Point out every Plasmodium parasite.
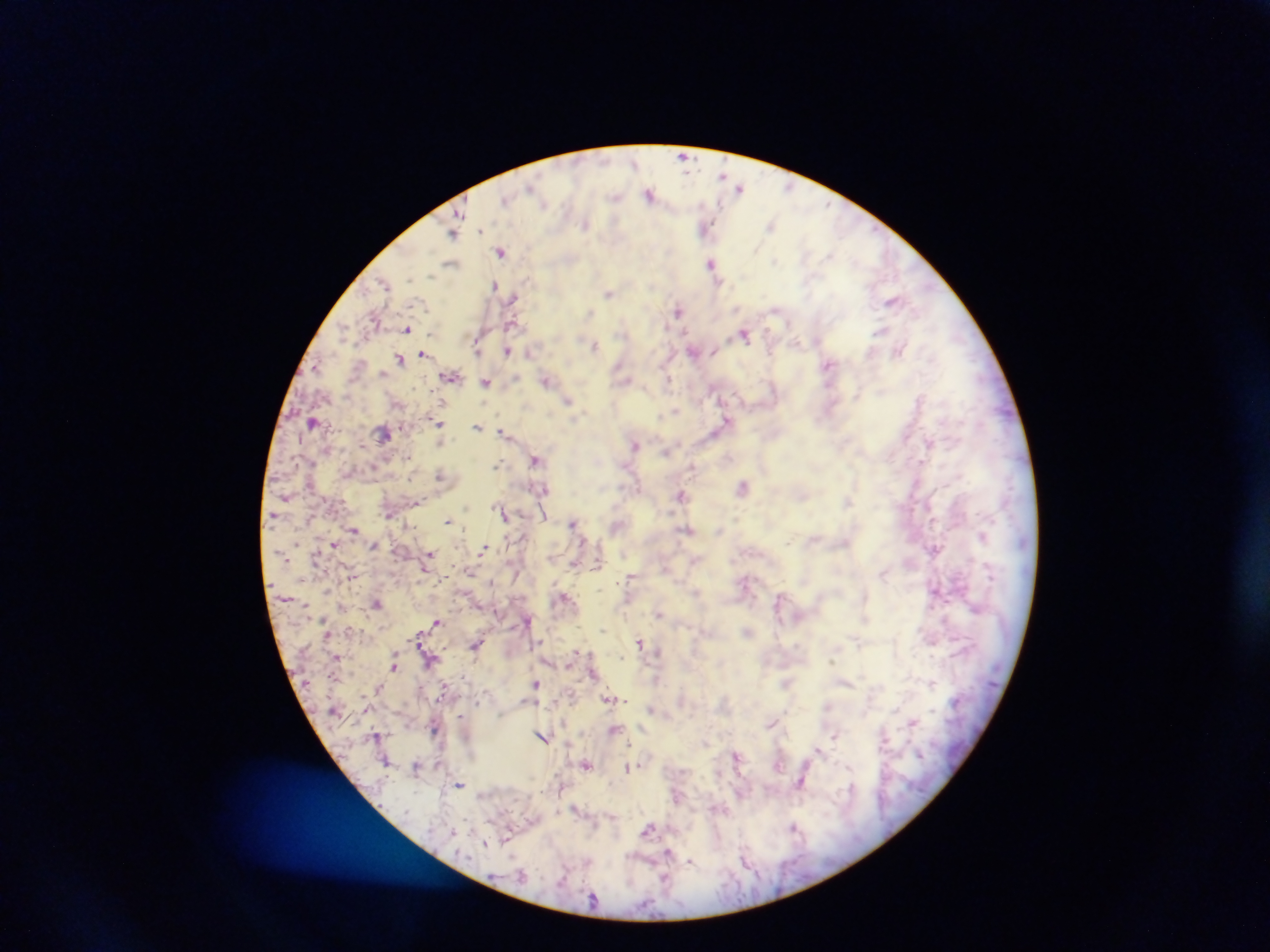

Approximate centers as (x, y) in pixels.
Plasmodium parasites: (684, 155), (634, 163), (722, 175), (789, 187), (740, 188), (650, 194), (615, 196), (827, 204), (585, 223), (771, 225), (706, 228), (453, 234), (502, 251), (775, 260), (712, 263), (451, 264), (430, 276), (384, 283), (494, 285), (609, 294), (512, 298), (892, 301), (737, 309), (775, 309), (679, 310), (589, 314), (511, 324), (406, 329), (881, 330), (743, 336), (595, 346), (507, 351), (899, 351), (530, 352), (694, 352), (423, 353), (400, 359), (829, 366), (316, 367), (451, 377), (667, 379), (546, 381), (485, 383), (857, 395), (568, 400), (675, 410), (727, 421), (438, 422), (477, 427), (503, 430), (929, 443), (635, 444), (666, 452), (407, 458), (535, 460), (496, 464), (692, 467), (440, 475), (743, 486), (680, 494), (847, 502), (504, 514), (447, 521), (573, 523), (354, 529), (686, 530), (788, 542), (334, 545), (484, 548), (430, 553), (631, 579), (376, 604), (659, 614), (437, 621), (603, 630), (540, 642), (640, 642), (476, 645), (657, 651), (577, 652), (622, 657), (831, 661), (394, 666), (536, 684), (608, 699), (625, 700), (771, 724), (834, 736), (542, 737), (629, 744), (818, 749), (586, 765), (628, 767), (801, 783), (459, 785), (793, 827), (648, 829), (507, 837), (485, 843), (668, 853), (690, 860).

{
  "field_of_view": "single",
  "image_size": "1270×952 pixels",
  "country": "Ghana",
  "preparation": "thick blood film",
  "capture": "mobile-phone photograph through a microscope",
  "leukocyte_locations": "approximate centers as (x, y) in pixels: (312, 419), (385, 433)"
}